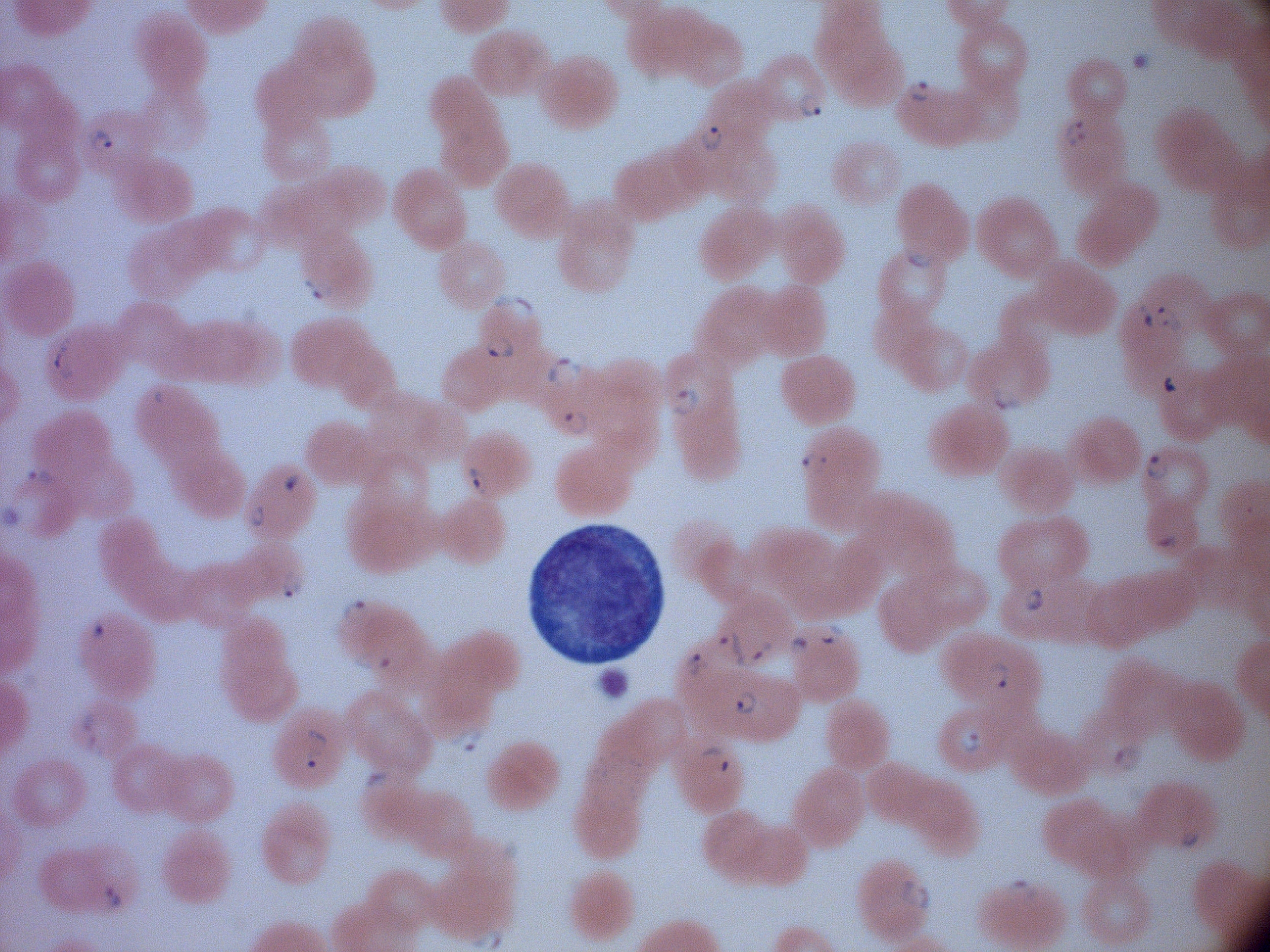

magnification = 100x
microscope = Leica DM2000 with built-in camera
field of view = one from this slide
ring form locations = approximate bounding boxes as (x1,y1)-(x2,y2) corner pairs in pixels, from the source annotation, which is not necessarily exhaustive: (906,76)-(934,103), (794,86)-(826,124), (1063,118)-(1088,148), (699,123)-(728,157), (85,129)-(114,155), (901,243)-(936,273), (305,274)-(334,302), (495,294)-(538,322), (1152,302)-(1183,332), (1135,304)-(1156,328), (480,332)-(517,358), (51,336)-(75,379), (545,357)-(585,388), (668,384)-(701,415), (986,384)-(1022,412), (558,406)-(596,437), (796,448)-(834,477), (1141,451)-(1170,481), (463,461)-(493,496), (26,466)-(58,489), (246,502)-(269,529), (278,572)-(304,601), (1024,585)-(1047,614), (340,597)-(370,625), (815,623)-(844,648), (714,630)-(748,670), (785,633)-(812,657), (748,638)-(779,669), (339,649)-(397,674), (681,649)-(711,677), (983,659)-(1011,690), (732,688)-(758,717), (77,704)-(102,744), (445,726)-(487,756), (956,726)-(984,759), (301,727)-(330,772), (84,738)-(109,762), (1108,741)-(1146,776), (361,769)-(395,793), (1175,826)-(1205,853), (895,876)-(935,916), (1001,878)-(1038,903)
stain = Giemsa
image size = 1270×952 pixels
preparation = thin blood film
species = Plasmodium falciparum